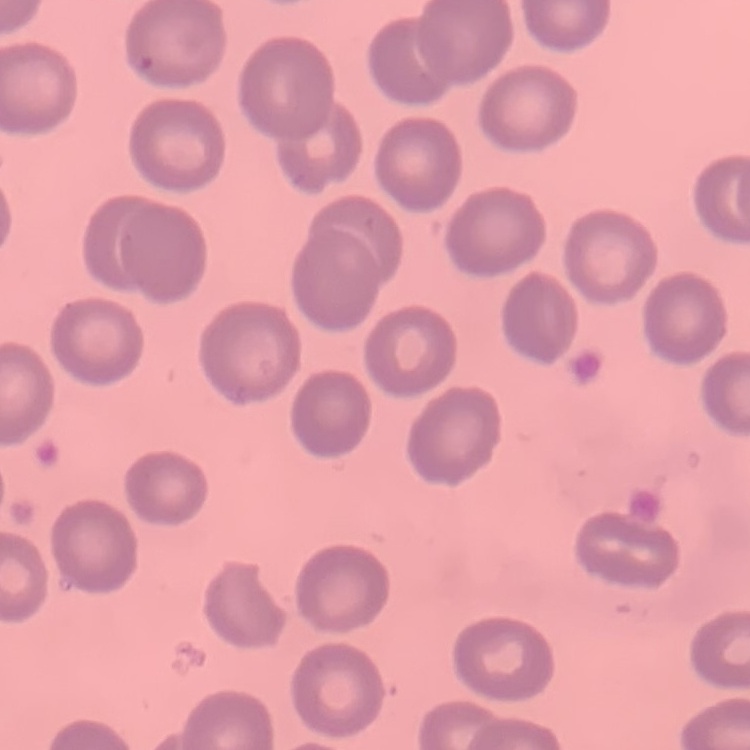

Summary:
  - Red blood cell morphology: no rouleaux formation
  - Stain: Field's or Giemsa
  - Image type: square crop of a larger photomicrograph
  - Preparation: thin peripheral smear